Report the malaria status of this cell.
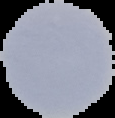

It is uninfected.

preparation = thin blood film
image size = 115×118 pixels
image type = cell region segmented out of the field of view; surrounding area masked to black